Assess this cell for malaria.
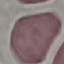
It is uninfected.

Summary:
  - Preparation: thin blood film
  - Capture: smartphone through the microscope eyepiece
  - Stain: Giemsa
  - Image type: automatically extracted cell patch, resized to 64 × 64 pixels